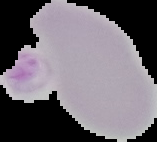
image_size: 157×142 pixels
malaria_status: uninfected
preparation: thin blood film
image_type: segmented cell region on a black background